Locate and identify every blood parasite.
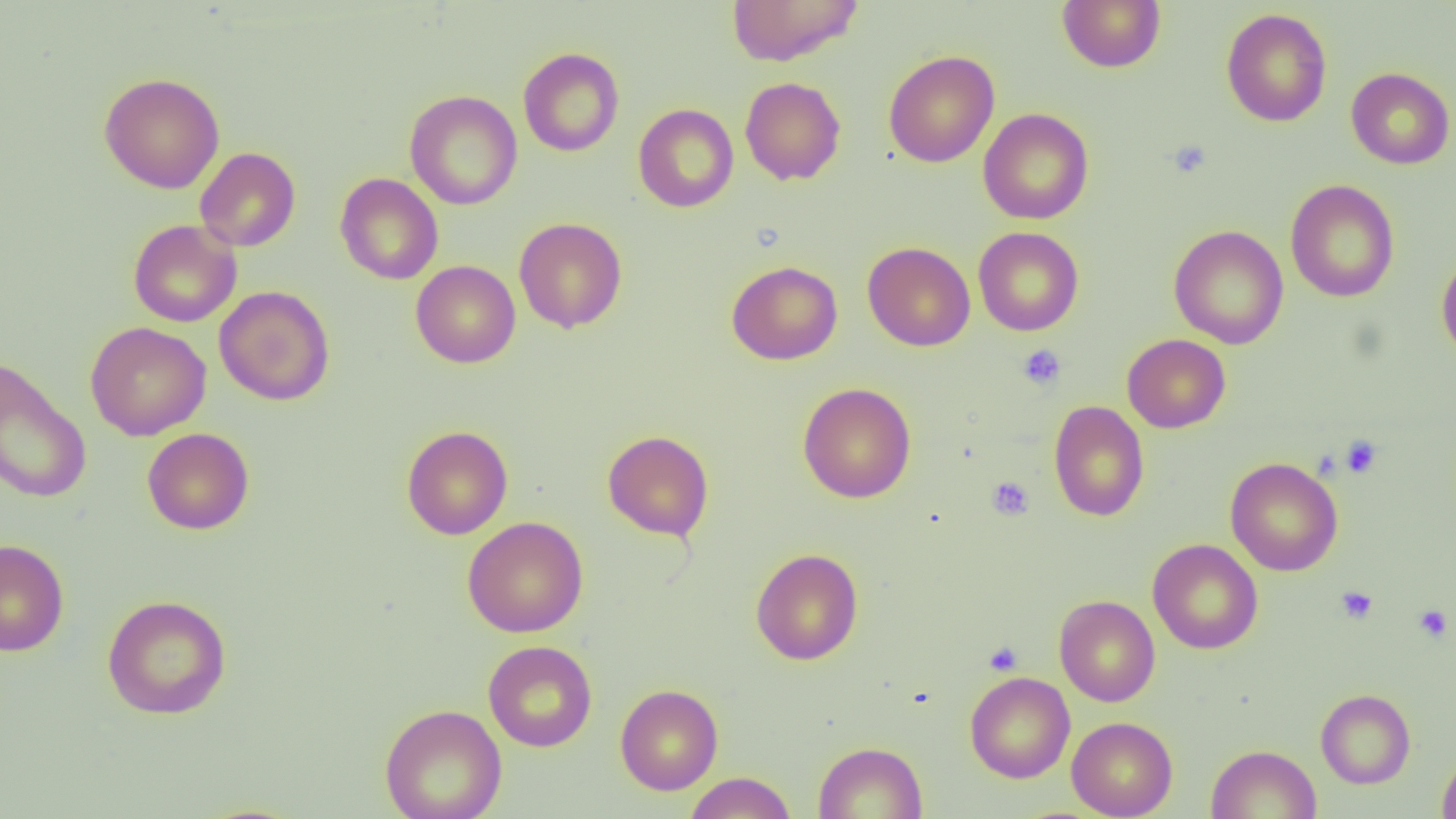
No blood parasites seen.

slide_level_diagnosis: no evidence of blood parasites
image_size: 1456×819 pixels
platelet_locations: 'approximate bounding boxes as named x1/y1/x2/y2 corners in pixels: (x1=1166, y1=140, x2=1211, y2=179), (x1=1017, y1=344, x2=1065, y2=389), (x1=1341, y1=435, x2=1382, y2=478), (x1=987, y1=477, x2=1034, y2=520), (x1=1335, y1=586, x2=1378, y2=624), (x1=1413, y1=604, x2=1453, y2=643), (x1=983, y1=640, x2=1023, y2=675)'
modality: light microscopy
field_of_view: one of a larger specimen
magnification: 1000x
preparation: thin blood smear
uninfected_red_blood_cell_locations: 'approximate bounding boxes as named x1/y1/x2/y2 corners in pixels: (x1=727, y1=0, x2=864, y2=66), (x1=1057, y1=0, x2=1165, y2=72), (x1=1221, y1=8, x2=1332, y2=127), (x1=518, y1=47, x2=624, y2=156), (x1=883, y1=49, x2=999, y2=168), (x1=1346, y1=67, x2=1455, y2=169), (x1=99, y1=72, x2=225, y2=194), (x1=740, y1=76, x2=846, y2=185), (x1=404, y1=90, x2=522, y2=210), (x1=633, y1=104, x2=738, y2=212), (x1=978, y1=107, x2=1093, y2=224), (x1=195, y1=147, x2=300, y2=251), (x1=335, y1=173, x2=444, y2=285), (x1=1285, y1=179, x2=1400, y2=302), (x1=514, y1=217, x2=627, y2=333), (x1=128, y1=219, x2=242, y2=327), (x1=1169, y1=224, x2=1288, y2=349), (x1=973, y1=227, x2=1083, y2=336), (x1=862, y1=241, x2=975, y2=351), (x1=1436, y1=252, x2=1456, y2=363), (x1=411, y1=260, x2=521, y2=368), (x1=726, y1=260, x2=842, y2=365), (x1=214, y1=285, x2=335, y2=406), (x1=85, y1=322, x2=211, y2=441), (x1=1122, y1=334, x2=1231, y2=433), (x1=0, y1=356, x2=92, y2=504), (x1=798, y1=382, x2=916, y2=504), (x1=1048, y1=400, x2=1149, y2=521), (x1=401, y1=425, x2=513, y2=540), (x1=142, y1=428, x2=254, y2=534), (x1=602, y1=430, x2=714, y2=541), (x1=1225, y1=457, x2=1343, y2=576), (x1=462, y1=516, x2=588, y2=637), (x1=0, y1=539, x2=69, y2=656), (x1=1148, y1=539, x2=1263, y2=654), (x1=751, y1=548, x2=863, y2=666), (x1=102, y1=594, x2=232, y2=720), (x1=1054, y1=595, x2=1160, y2=706), (x1=483, y1=640, x2=598, y2=752), (x1=964, y1=671, x2=1075, y2=783), (x1=615, y1=684, x2=723, y2=795), (x1=1315, y1=689, x2=1416, y2=788), (x1=379, y1=703, x2=507, y2=819), (x1=1067, y1=716, x2=1178, y2=818), (x1=812, y1=741, x2=928, y2=819), (x1=1205, y1=744, x2=1322, y2=819), (x1=1437, y1=751, x2=1456, y2=819), (x1=684, y1=771, x2=797, y2=818)'